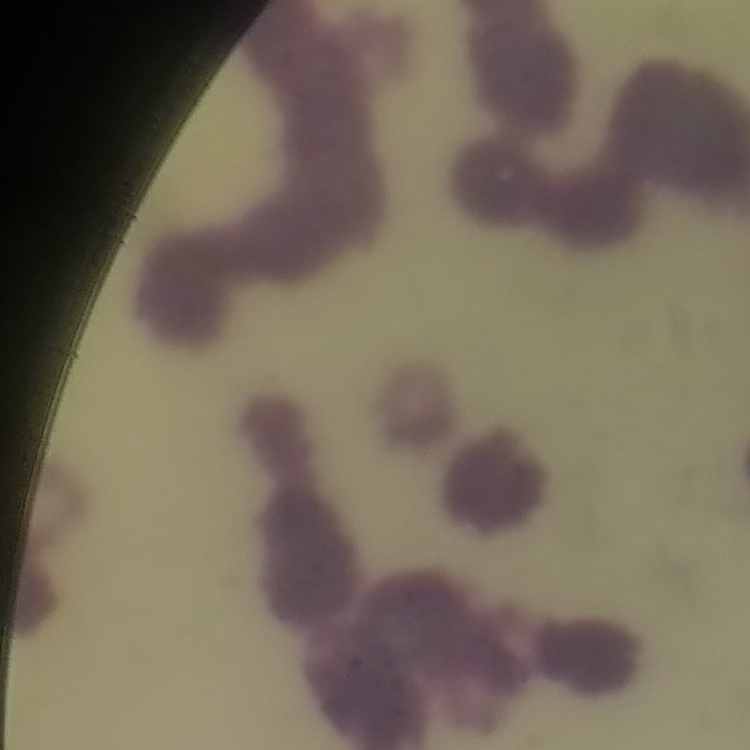

red blood cell morphology = rouleaux formation
image type = square crop of a larger photomicrograph
stain = Field's or Giemsa
preparation = thin blood smear